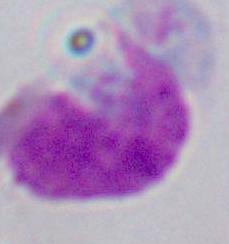

Summary:
  - Identification: white blood cell
  - Magnification: 1000x
  - Modality: micrograph